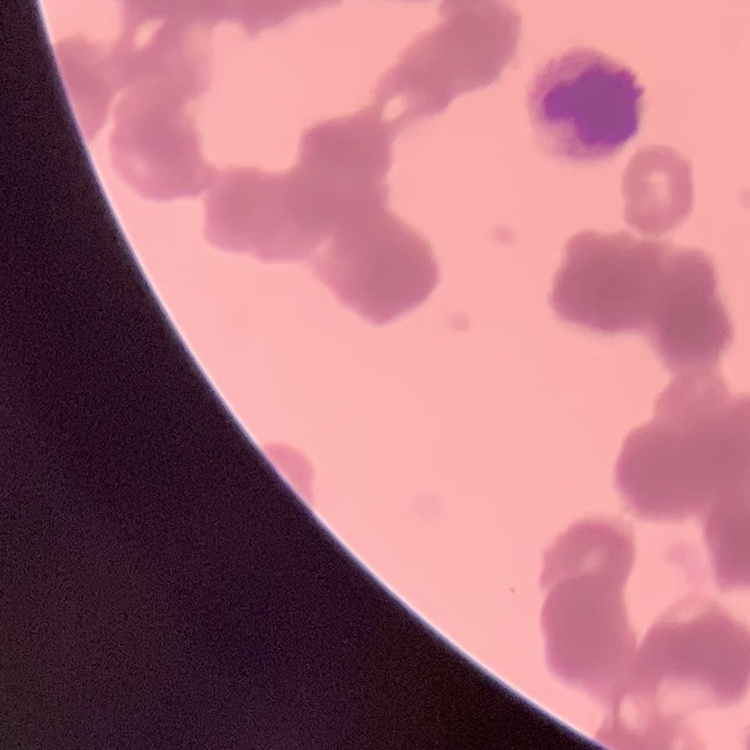 The erythrocytes exhibit rouleaux formation. Thin blood smear. One tile cut from a larger photomicrograph. Stained with either Field's or Giemsa.